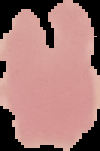
The area outside the segmented cell region is set to black. Malaria status: uninfected. From a thin blood smear. Image is 100×151 pixels.